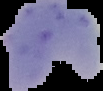
Summary:
  - Image type: segmented cell region on a black background
  - Image size: 103×91 pixels
  - Result: malaria parasites identified
  - Preparation: thin blood smear